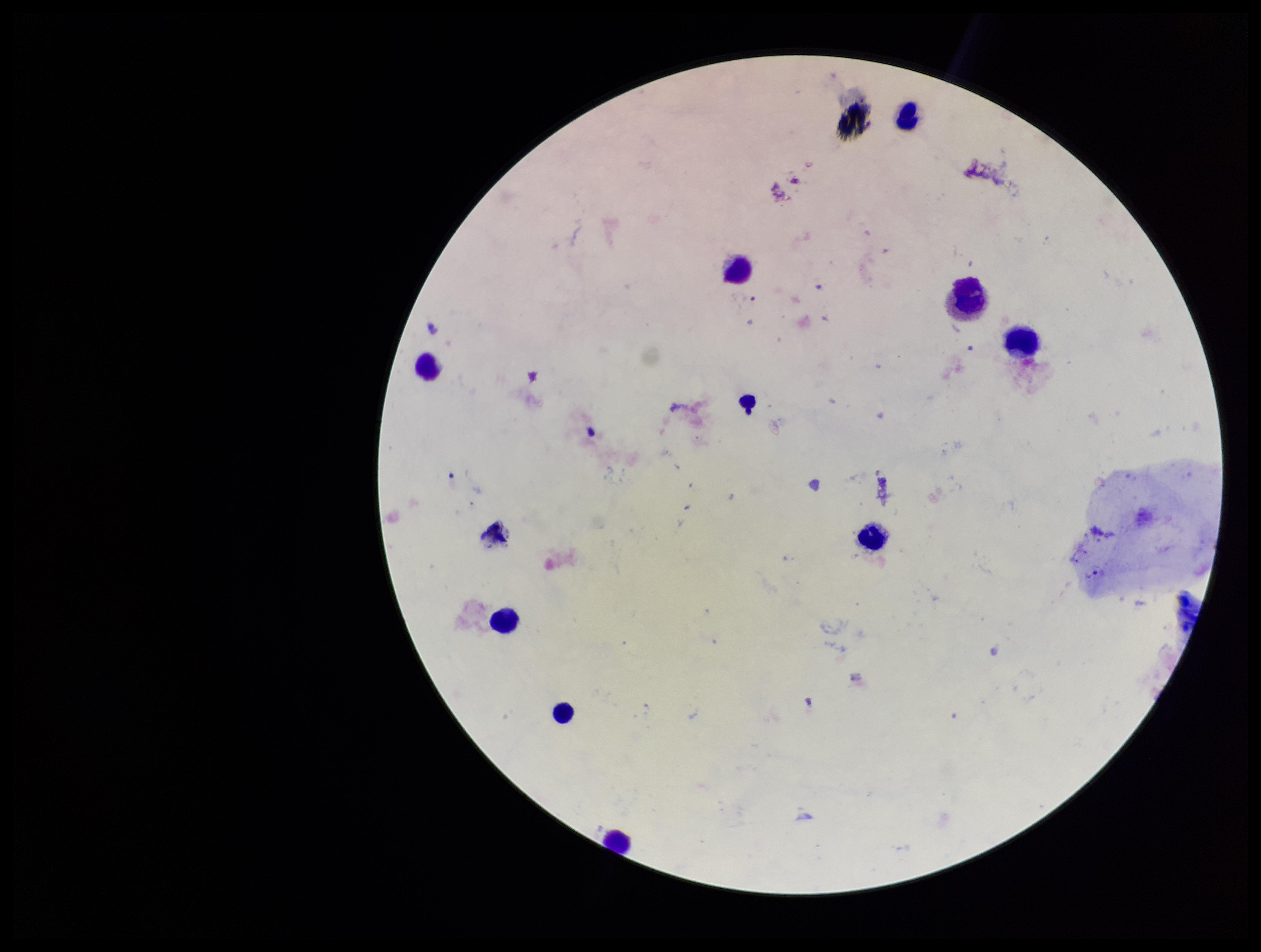
leukocyte count = 9
stain = Giemsa
capture = smartphone photograph through the microscope eyepiece
parasite count = 0
preparation = thick smear
patient malaria status = negative
Plasmodium parasites = none seen
field of view = single
image size = 1261×952 pixels